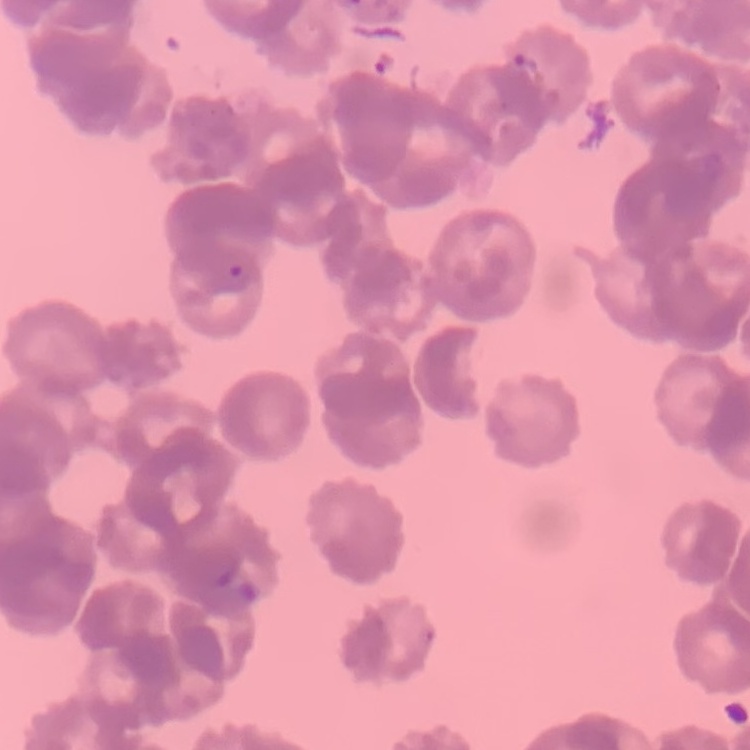 The erythrocytes exhibit rouleaux formation. Field's or Giemsa stain. Square crop of a larger photomicrograph. Thin blood film.